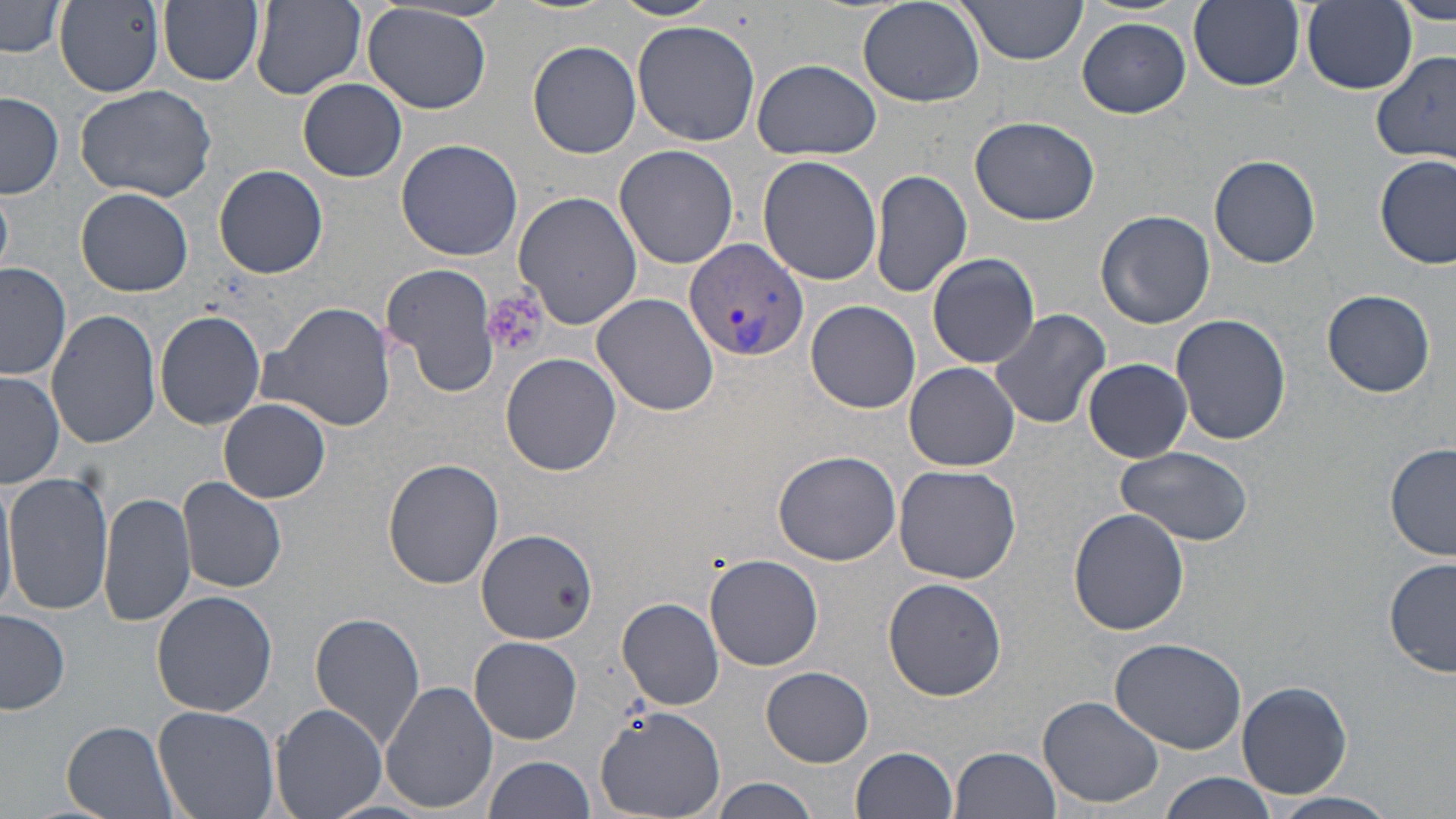
Summary:
  - Coordinate format: approximate bounding boxes as named x1/y1/x2/y2 corners in pixels
  - Uninfected red blood cell locations: (x1=157, y1=0, x2=264, y2=86), (x1=610, y1=0, x2=722, y2=22), (x1=857, y1=0, x2=985, y2=108), (x1=1189, y1=0, x2=1304, y2=91), (x1=1299, y1=0, x2=1417, y2=94), (x1=1390, y1=0, x2=1456, y2=25), (x1=1, y1=1, x2=66, y2=58), (x1=54, y1=1, x2=165, y2=97), (x1=252, y1=1, x2=367, y2=98), (x1=955, y1=1, x2=1089, y2=64), (x1=362, y1=4, x2=493, y2=114), (x1=1077, y1=17, x2=1191, y2=118), (x1=632, y1=21, x2=762, y2=146), (x1=528, y1=40, x2=642, y2=159), (x1=1370, y1=49, x2=1456, y2=163), (x1=752, y1=58, x2=881, y2=160), (x1=298, y1=78, x2=407, y2=182), (x1=74, y1=84, x2=218, y2=203), (x1=1, y1=91, x2=65, y2=199), (x1=970, y1=114, x2=1099, y2=226), (x1=395, y1=138, x2=523, y2=261), (x1=614, y1=144, x2=739, y2=269), (x1=1210, y1=154, x2=1321, y2=267), (x1=1375, y1=154, x2=1454, y2=270), (x1=758, y1=155, x2=884, y2=286), (x1=214, y1=164, x2=328, y2=278), (x1=870, y1=170, x2=972, y2=298), (x1=0, y1=184, x2=15, y2=274), (x1=76, y1=187, x2=195, y2=296), (x1=512, y1=191, x2=643, y2=329), (x1=1096, y1=210, x2=1215, y2=329), (x1=925, y1=251, x2=1041, y2=368), (x1=939, y1=257, x2=1087, y2=416), (x1=1, y1=262, x2=72, y2=383), (x1=381, y1=263, x2=502, y2=394), (x1=1322, y1=289, x2=1436, y2=397), (x1=591, y1=292, x2=721, y2=415), (x1=806, y1=300, x2=921, y2=413), (x1=261, y1=301, x2=395, y2=433), (x1=989, y1=308, x2=1111, y2=431), (x1=45, y1=310, x2=162, y2=449), (x1=154, y1=311, x2=264, y2=429), (x1=1171, y1=313, x2=1290, y2=446), (x1=500, y1=352, x2=623, y2=476), (x1=1083, y1=357, x2=1192, y2=462), (x1=904, y1=362, x2=1020, y2=472), (x1=1, y1=373, x2=65, y2=489), (x1=219, y1=399, x2=330, y2=503), (x1=1385, y1=444, x2=1456, y2=562), (x1=1116, y1=446, x2=1253, y2=547), (x1=771, y1=449, x2=903, y2=568), (x1=382, y1=458, x2=504, y2=590), (x1=892, y1=465, x2=1022, y2=584), (x1=0, y1=472, x2=17, y2=615), (x1=3, y1=472, x2=113, y2=616), (x1=177, y1=476, x2=288, y2=593), (x1=99, y1=491, x2=195, y2=628), (x1=1069, y1=507, x2=1191, y2=635), (x1=476, y1=528, x2=596, y2=643), (x1=705, y1=554, x2=824, y2=672), (x1=1385, y1=558, x2=1455, y2=679), (x1=882, y1=576, x2=1006, y2=700), (x1=151, y1=590, x2=277, y2=717), (x1=616, y1=598, x2=726, y2=711), (x1=0, y1=610, x2=72, y2=715), (x1=311, y1=611, x2=427, y2=750), (x1=470, y1=636, x2=583, y2=744), (x1=1108, y1=637, x2=1247, y2=753), (x1=762, y1=666, x2=874, y2=766), (x1=380, y1=679, x2=499, y2=814), (x1=1237, y1=680, x2=1354, y2=799), (x1=1038, y1=694, x2=1167, y2=807), (x1=270, y1=701, x2=389, y2=819), (x1=595, y1=704, x2=727, y2=816), (x1=154, y1=705, x2=279, y2=819), (x1=61, y1=719, x2=184, y2=819), (x1=850, y1=746, x2=959, y2=819), (x1=949, y1=746, x2=1062, y2=819), (x1=481, y1=754, x2=595, y2=819), (x1=1158, y1=771, x2=1276, y2=819), (x1=711, y1=777, x2=824, y2=819), (x1=1272, y1=792, x2=1400, y2=816)
  - Plasmodium vivax-infected red blood cell locations: (x1=686, y1=237, x2=807, y2=361)
  - Platelet locations: (x1=484, y1=290, x2=548, y2=359)
  - Slide-level diagnosis: Plasmodium vivax
  - Stain: May-Grünwald-Giemsa
  - Image size: 1456×819 pixels
  - Preparation: thin blood film
  - Modality: optical microscopy
  - Magnification: 1000x
  - Field of view: single